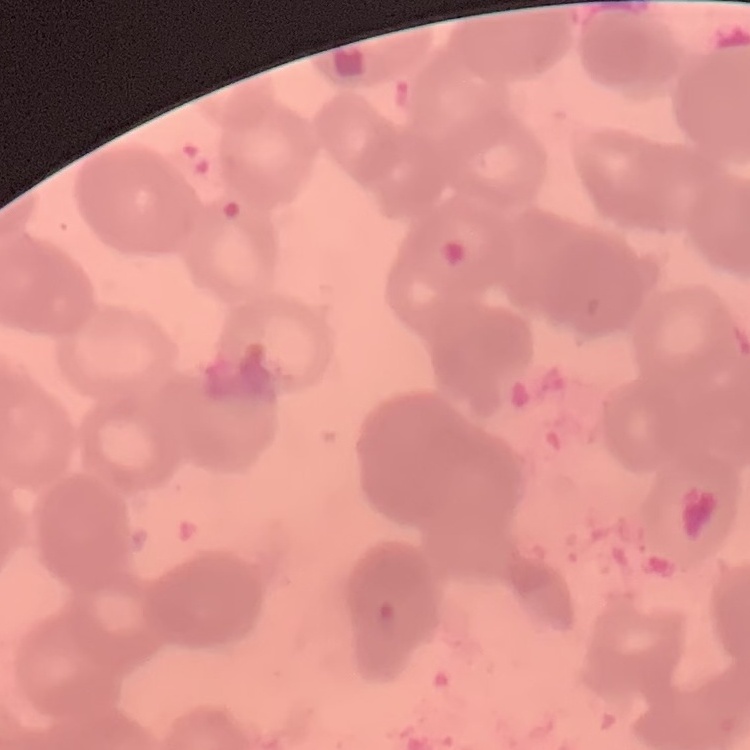

Summary:
  - Red blood cell morphology: rouleaux formation
  - Preparation: thin blood film
  - Image type: square crop of a larger photomicrograph
  - Stain: Field's or Giemsa